Locate every blood parasite and identify its species.
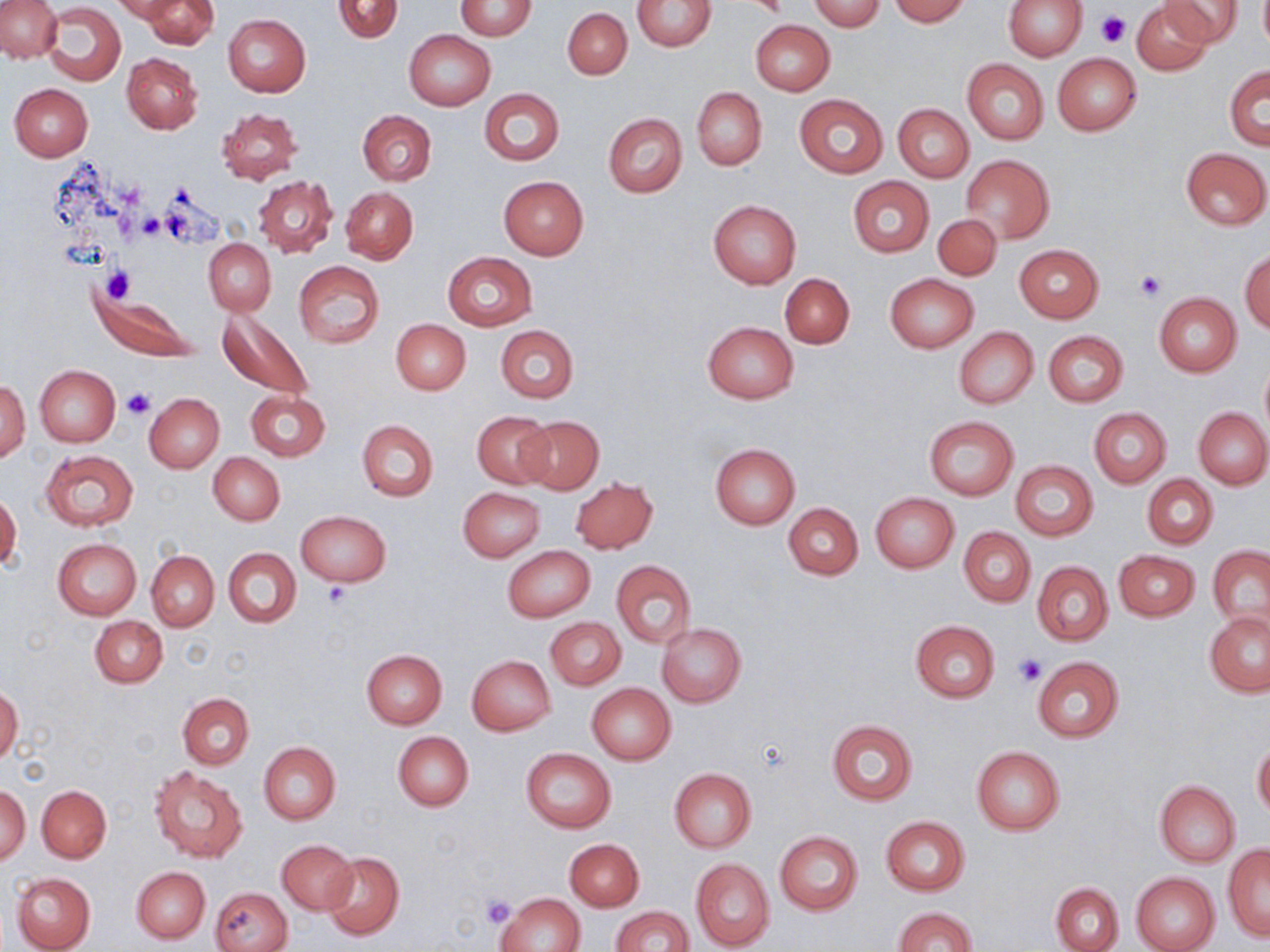
No blood parasites observed.

Summary:
  - Coordinate format: approximate bounding boxes as [x1, y1, x2, y2] in pixels
  - Uninfected red blood cell locations: [0, 0, 62, 61], [113, 0, 191, 23], [141, 0, 217, 50], [332, 0, 403, 43], [809, 0, 884, 32], [888, 0, 970, 24], [1003, 0, 1085, 60], [1131, 0, 1213, 75], [1160, 0, 1244, 48], [454, 1, 537, 39], [633, 1, 716, 51], [44, 4, 125, 86], [563, 8, 632, 79], [223, 14, 310, 97], [750, 20, 835, 96], [404, 29, 496, 111], [122, 52, 202, 134], [1052, 53, 1142, 135], [962, 58, 1048, 145], [1225, 66, 1269, 150], [11, 84, 93, 161], [479, 88, 566, 165], [692, 88, 767, 169], [794, 94, 888, 179], [893, 104, 973, 183], [216, 107, 301, 185], [358, 110, 436, 186], [603, 113, 687, 197], [1181, 149, 1269, 230], [962, 155, 1054, 242], [253, 176, 337, 258], [498, 176, 589, 260], [848, 176, 934, 258], [341, 187, 417, 264], [707, 199, 802, 288], [932, 214, 1002, 281], [204, 239, 276, 315], [1014, 245, 1102, 322], [1240, 250, 1269, 333], [442, 251, 537, 331], [293, 262, 384, 348], [781, 274, 855, 348], [886, 274, 977, 352], [94, 291, 202, 363], [1154, 293, 1242, 378], [218, 310, 312, 401], [392, 320, 471, 395], [703, 321, 798, 403], [495, 324, 578, 404], [954, 327, 1038, 409], [1043, 331, 1127, 407], [1260, 362, 1270, 434], [34, 365, 119, 446], [1, 381, 30, 461], [245, 389, 330, 461], [144, 393, 224, 471], [1089, 408, 1171, 486], [1194, 408, 1270, 488], [473, 411, 554, 488], [925, 416, 1019, 499], [518, 417, 604, 495], [357, 419, 438, 501], [710, 444, 800, 528], [41, 450, 138, 530], [209, 453, 285, 525], [1010, 460, 1098, 541], [1143, 475, 1218, 550], [570, 477, 658, 553], [458, 488, 544, 561], [871, 493, 958, 572], [0, 494, 21, 569], [783, 504, 863, 580], [296, 510, 390, 587], [958, 528, 1034, 606], [53, 538, 141, 620], [502, 545, 595, 622], [1208, 545, 1270, 633], [224, 547, 302, 628], [1114, 549, 1200, 622], [147, 551, 219, 631], [612, 560, 696, 648], [1032, 562, 1113, 645], [1204, 612, 1270, 696], [90, 615, 167, 688], [545, 617, 626, 690], [911, 620, 999, 703], [656, 622, 746, 707], [360, 649, 447, 729], [467, 655, 555, 736], [1033, 659, 1124, 741], [586, 682, 676, 765], [0, 685, 23, 766], [179, 693, 254, 770], [826, 720, 918, 804], [392, 731, 474, 811], [1252, 740, 1270, 818], [258, 742, 339, 824], [971, 745, 1065, 835], [520, 747, 616, 834], [149, 765, 247, 862], [669, 768, 757, 852], [1154, 781, 1240, 866], [0, 784, 30, 865], [37, 785, 111, 863], [881, 816, 969, 896], [775, 831, 864, 915], [565, 839, 644, 911], [277, 840, 358, 914], [1222, 845, 1270, 940], [322, 850, 404, 942], [691, 859, 774, 950], [132, 866, 210, 944], [11, 871, 96, 952], [1130, 872, 1220, 952], [1051, 882, 1122, 952], [209, 886, 292, 952], [497, 892, 583, 952], [610, 905, 694, 952], [892, 906, 978, 952]
  - Platelet locations: [1098, 10, 1128, 47], [139, 214, 166, 240], [102, 265, 136, 303], [1134, 270, 1164, 302], [121, 388, 156, 419], [324, 582, 352, 607], [1012, 652, 1046, 687], [480, 893, 515, 927]
  - Slide-level diagnosis: negative for blood parasites
  - Preparation: thin blood smear
  - Stain: May-Grünwald-Giemsa
  - Magnification: 1000x
  - Field of view: one of a larger specimen
  - Modality: optical microscopy
  - Image size: 1270×952 pixels